Locate every malaria parasite.
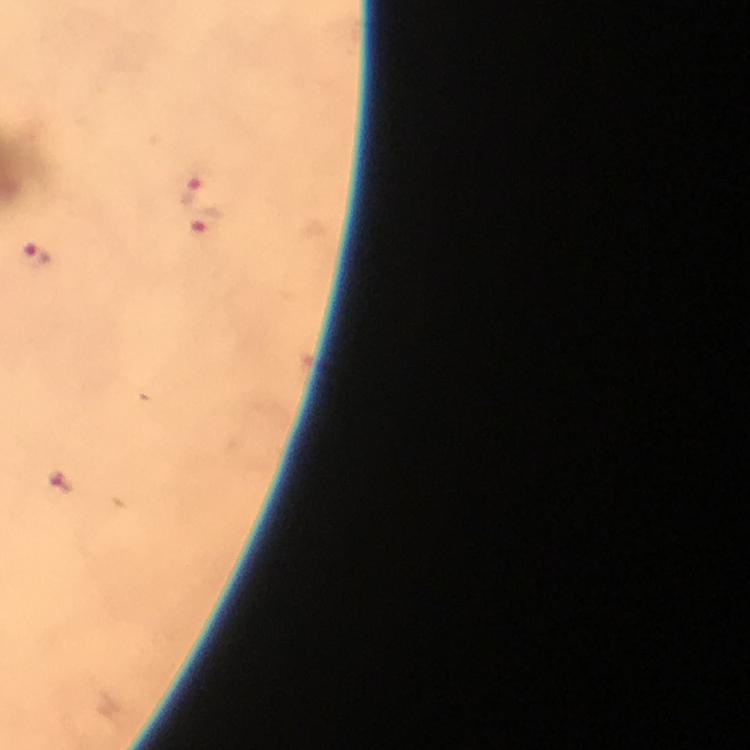
Approximate centers as (x, y) in pixels.
Malaria parasites: (192, 189), (208, 224), (35, 257), (59, 481).

Immersion oil applied. Cropped region of a single field of view. Smartphone photograph taken through a microscope. Image is 750×750 pixels. At 100x magnification. Giemsa-stained preparation. Thick smear. From a malaria diagnostic workup.